State which parasite is depicted.
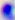

Toxoplasma gondii.

Summary:
  - Modality: photomicrograph
  - Magnification: 400x